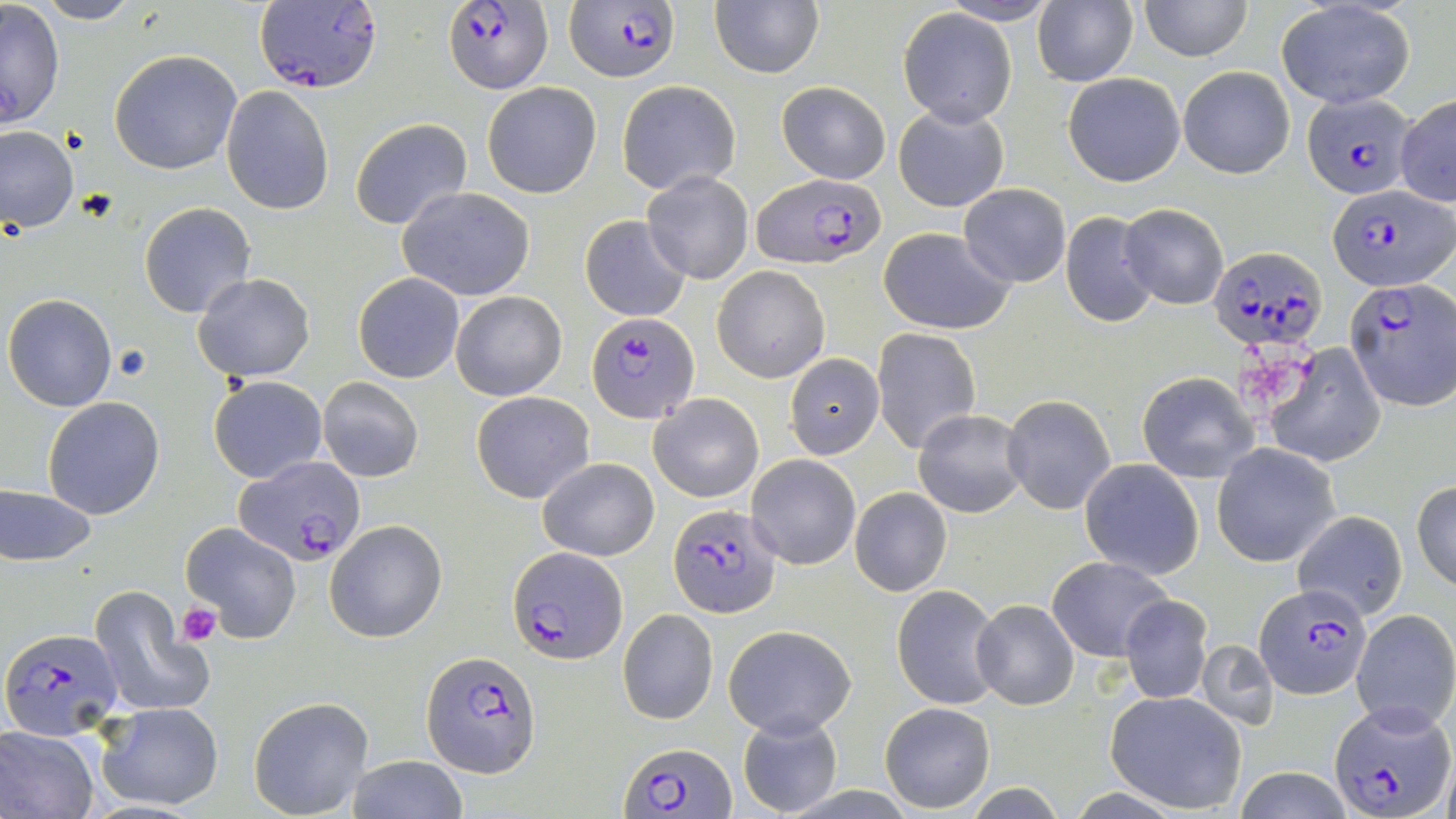

slide-level diagnosis = Plasmodium falciparum
modality = light microscopy
platelet locations = approximate bounding boxes as (x1,y1)-(x2,y2) corner pairs in pixels: (1237,346)-(1304,410), (178,604)-(221,646)
image size = 1456×819 pixels
magnification = 1000x
uninfected red blood cell locations = approximate bounding boxes as (x1,y1)-(x2,y2) corner pairs in pixels: (710,0)-(824,79), (1139,0)-(1252,61), (1,1)-(66,132), (35,1)-(143,25), (939,1)-(1060,25), (1031,1)-(1138,87), (1276,2)-(1416,110), (898,9)-(1017,127), (108,50)-(242,174), (1178,66)-(1295,179), (1062,71)-(1187,187), (616,80)-(741,195), (775,80)-(891,184), (482,81)-(602,198), (221,86)-(335,215), (1395,95)-(1456,207), (893,103)-(1010,212), (349,118)-(473,231), (0,124)-(78,232), (642,171)-(755,284), (958,183)-(1072,287), (397,186)-(536,302), (139,203)-(256,318), (1120,204)-(1228,310), (1060,209)-(1158,327), (579,214)-(691,322), (877,226)-(1016,335), (714,265)-(829,381), (354,272)-(465,384), (192,273)-(315,382), (451,290)-(567,401), (3,293)-(117,411), (872,328)-(982,454), (1265,344)-(1386,467), (785,354)-(885,458), (1136,371)-(1258,483), (209,375)-(327,484), (317,377)-(424,483), (471,391)-(595,502), (648,393)-(762,503), (1003,394)-(1117,515), (42,397)-(164,519), (914,409)-(1031,517), (1212,444)-(1339,567), (748,454)-(860,570), (538,458)-(658,561), (1081,459)-(1202,578), (1412,479)-(1456,593), (0,485)-(97,566), (848,486)-(953,597), (1293,510)-(1409,620), (325,520)-(447,642), (181,523)-(302,643), (1048,556)-(1174,661), (892,583)-(1002,711), (88,587)-(211,719), (1120,595)-(1212,705), (970,599)-(1079,710), (618,608)-(718,724), (1352,609)-(1456,732), (725,625)-(853,737), (1197,640)-(1280,731), (1104,691)-(1248,814), (248,697)-(373,818), (880,701)-(996,812), (97,702)-(225,812), (736,712)-(844,817), (0,726)-(100,819), (348,755)-(470,818), (1228,768)-(1360,818)
preparation = thin blood film
Plasmodium falciparum-infected red blood cell locations = approximate bounding boxes as (x1,y1)-(x2,y2) corner pairs in pixels: (443,0)-(551,92), (566,0)-(682,82), (254,1)-(384,93), (1301,93)-(1416,199), (755,172)-(886,269), (1326,184)-(1451,291), (1209,244)-(1328,351), (1343,277)-(1456,411), (587,312)-(698,423), (234,456)-(367,568), (669,506)-(781,618), (508,546)-(625,663), (1255,583)-(1372,698), (1,627)-(122,740), (422,649)-(540,778), (1331,704)-(1454,817), (620,741)-(736,818)
field of view = single
stain = May-Grünwald-Giemsa